Classify this cell by malaria status.
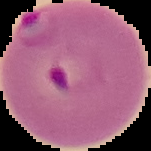

Parasitized.

image size = 151×151 pixels
preparation = thin blood smear
image type = segmented cell region on a black background